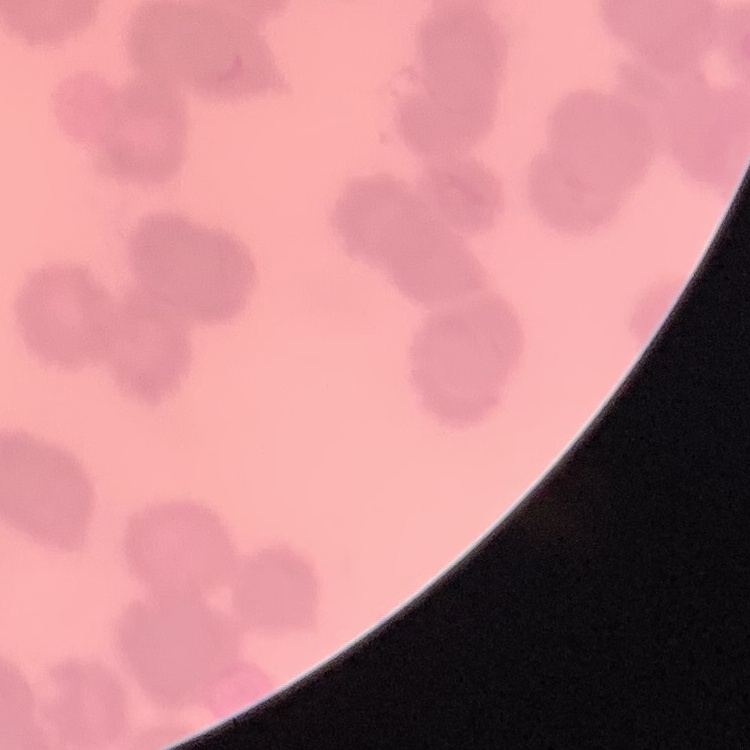
Summary:
  - Red blood cell morphology: rouleaux formation
  - Image type: square crop of a larger photomicrograph
  - Preparation: thin blood film
  - Stain: Field's or Giemsa